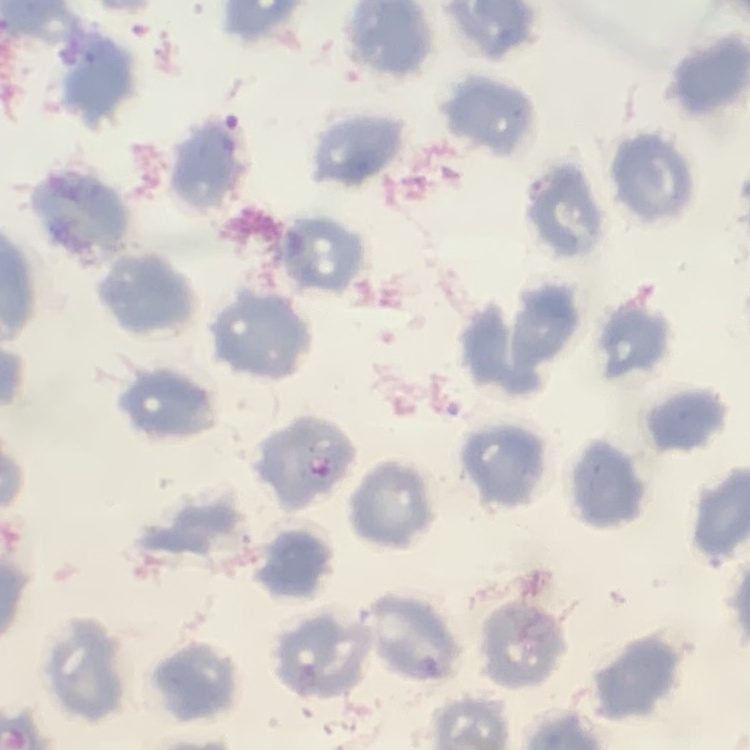

The red blood cells exhibit no rouleaux formation. Square crop of a larger photomicrograph. Field's or Giemsa stain. Thin blood film.